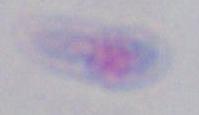 Toxoplasma gondii is shown. Captured at 1000x magnification. Micrograph.